Report the malaria status of this cell.
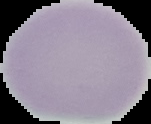

Uninfected.

{
  "image_size": "151×124 pixels",
  "image_type": "segmented cell region with the area outside set to black",
  "preparation": "thin blood smear"
}